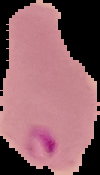

Image is 100×175 pixels. From a thin blood smear. Cell region segmented out of the field of view; the surrounding area is masked to black. Malaria status: parasitized.